Assess this cell for malaria.
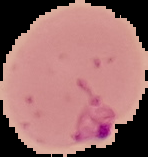
Parasitized.

preparation = thin blood film
image type = cell region segmented out of the field of view; surrounding area masked to black
image size = 148×157 pixels